Name the parasite shown.
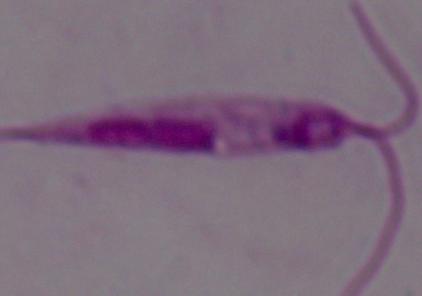
This is Leishmania.

Summary:
  - Magnification: 1000x
  - Modality: micrograph